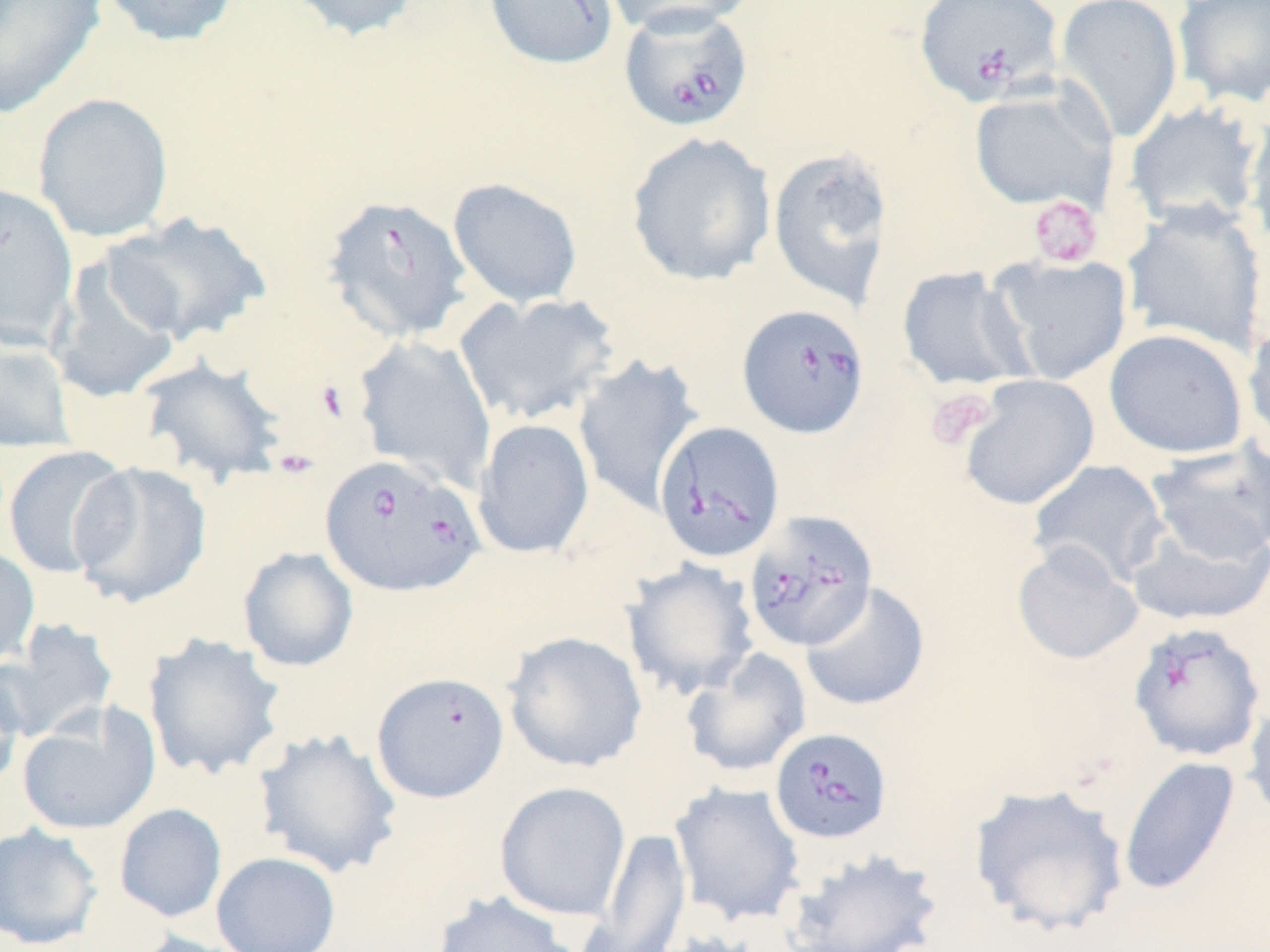
slide-level diagnosis = Babesia divergens
preparation = thin blood smear
field of view = one of a larger specimen
image size = 1270×952 pixels
uninfected red blood cell locations = approximate bounding boxes as (x1, y1, x2, y2) in pixels: (96, 0, 241, 48), (283, 0, 424, 42), (598, 0, 758, 36), (1054, 0, 1184, 143), (1172, 0, 1270, 109), (0, 1, 108, 120), (969, 84, 1116, 212), (32, 92, 174, 243), (1123, 101, 1264, 233), (1243, 106, 1270, 254), (625, 132, 777, 287), (767, 144, 896, 311), (447, 178, 583, 308), (0, 180, 79, 349), (1122, 200, 1269, 357), (101, 211, 274, 345), (47, 253, 185, 404), (989, 254, 1133, 385), (897, 267, 1034, 392), (454, 291, 621, 426), (1243, 317, 1270, 451), (1104, 328, 1249, 459), (0, 335, 77, 453), (353, 335, 497, 491), (571, 355, 704, 514), (137, 356, 288, 485), (957, 374, 1100, 511), (473, 419, 595, 559), (1144, 440, 1270, 567), (3, 444, 134, 580), (1027, 459, 1170, 588), (68, 461, 212, 609), (1125, 516, 1270, 628), (1011, 542, 1144, 666), (0, 544, 40, 669), (238, 546, 359, 673), (620, 558, 760, 700), (800, 580, 931, 712), (2, 619, 119, 743), (502, 630, 649, 773), (143, 633, 286, 780), (681, 647, 812, 778), (0, 657, 27, 794), (371, 671, 510, 803), (1242, 695, 1270, 826), (16, 704, 161, 835), (251, 727, 403, 879), (1118, 755, 1242, 897), (494, 781, 631, 921), (669, 781, 806, 927), (968, 782, 1130, 937), (114, 803, 228, 923), (0, 821, 104, 951), (581, 827, 693, 950), (780, 846, 946, 951), (211, 851, 341, 952), (430, 889, 581, 952), (130, 930, 257, 952)
modality = light microscopy
Babesia divergens-infected red blood cell locations = approximate bounding boxes as (x1, y1, x2, y2) in pixels: (483, 0, 619, 70), (914, 0, 1064, 105), (621, 2, 757, 130), (322, 193, 473, 343), (737, 303, 869, 439), (654, 420, 785, 563), (319, 453, 486, 598), (741, 511, 879, 655), (1129, 622, 1267, 764), (770, 728, 894, 846)
stain = May-Grünwald-Giemsa
magnification = 1000x
platelet locations = approximate bounding boxes as (x1, y1, x2, y2) in pixels: (1028, 195, 1103, 268), (925, 387, 997, 450)